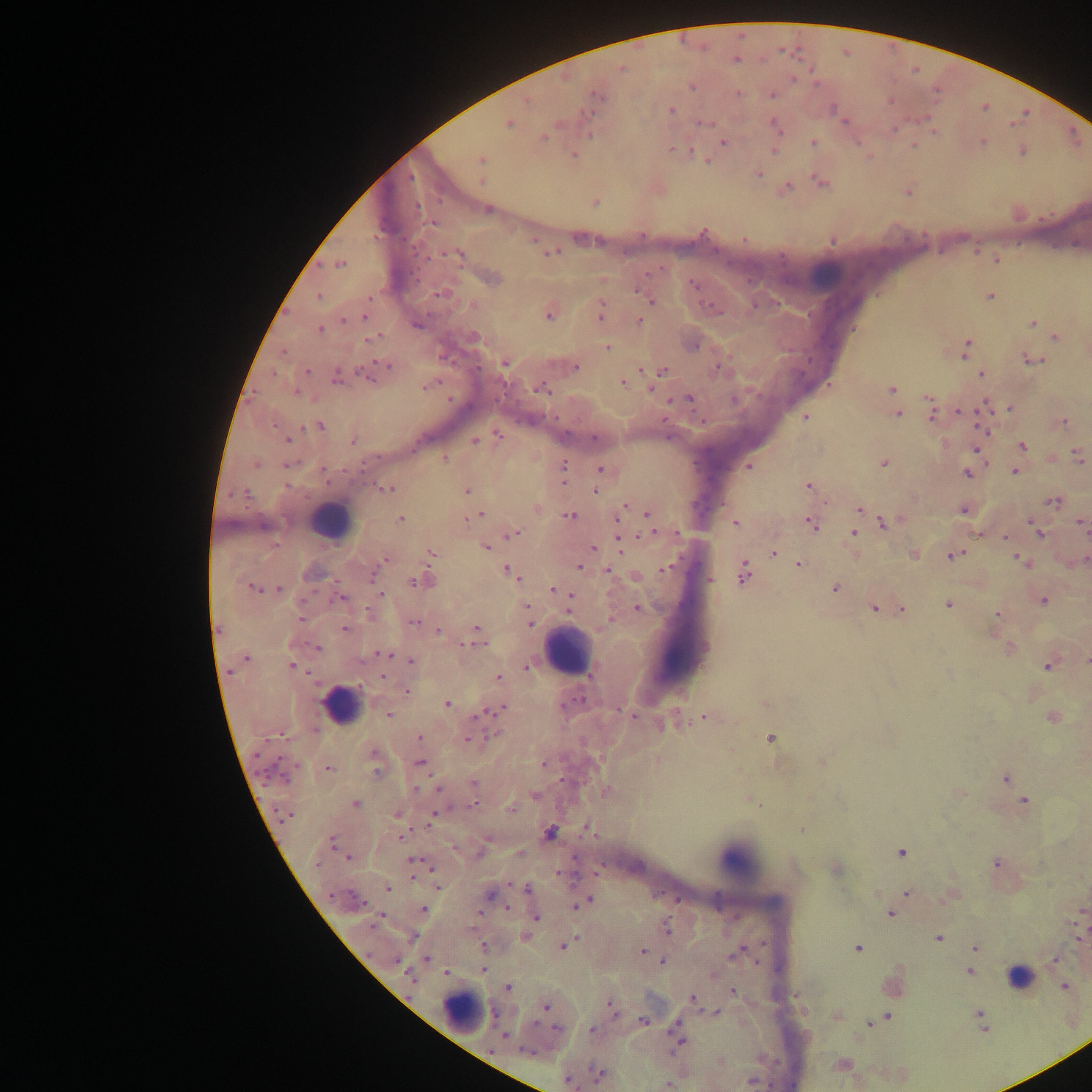 Approximate centers as [x, y] in pixels. Leukocyte locations: [819, 276], [330, 521], [568, 651], [340, 705], [739, 860], [1019, 979], [464, 1012]. Malaria parasite locations: [736, 60], [621, 68], [794, 79], [691, 87], [738, 93], [597, 95], [771, 95], [527, 101], [671, 109], [508, 123], [704, 123], [774, 125], [894, 129], [933, 129], [589, 135], [543, 138], [723, 143], [813, 143], [983, 143], [914, 145], [671, 149], [1021, 150], [773, 151], [574, 155], [480, 160], [707, 160], [760, 173], [821, 183], [787, 186], [595, 203], [487, 210], [433, 223], [703, 232], [744, 239], [551, 253], [459, 254], [995, 260], [340, 265], [653, 270], [493, 278], [694, 284], [442, 293], [641, 293], [319, 296], [989, 296], [649, 300], [548, 316], [601, 316], [364, 317], [344, 321], [639, 321], [1033, 322], [418, 325], [319, 329], [474, 336], [373, 338], [1055, 338], [695, 346], [607, 348], [966, 348], [283, 352], [1032, 360], [505, 363], [388, 366], [575, 367], [718, 368], [307, 371], [662, 371], [364, 373], [275, 375], [982, 375], [336, 379], [623, 382], [426, 386], [541, 388], [650, 388], [892, 390], [295, 392], [688, 399], [734, 400], [985, 405], [1009, 408], [960, 411], [898, 415], [932, 415], [805, 417], [1063, 422], [319, 426], [982, 433], [498, 435], [594, 437], [287, 440], [353, 441], [475, 441], [1023, 445], [976, 449], [1078, 456], [444, 459], [884, 462], [255, 464], [289, 465], [564, 466], [749, 467], [600, 470], [324, 471], [1015, 472], [967, 473], [807, 486], [387, 489], [466, 491], [595, 491], [244, 493], [1054, 501], [623, 507], [963, 510], [859, 511], [621, 512], [648, 513], [479, 515], [570, 515], [473, 516], [401, 520], [883, 521], [735, 523], [1083, 523], [812, 524], [618, 525], [676, 533], [854, 533], [1039, 533], [513, 534], [1005, 538], [619, 542], [485, 547], [593, 547], [773, 552], [431, 553], [954, 555], [1020, 560], [381, 563], [799, 565], [579, 567], [666, 568], [377, 569], [607, 570], [509, 571], [743, 573], [636, 577], [710, 580], [416, 582], [252, 588], [279, 589], [553, 589], [835, 589], [561, 592], [382, 594], [570, 596], [342, 597], [1043, 601], [948, 605], [637, 608], [874, 608], [901, 609], [527, 611], [997, 614], [301, 619], [414, 622], [530, 623], [476, 628], [344, 629], [219, 630], [438, 631], [471, 645], [318, 648], [386, 654], [246, 658], [411, 661], [1086, 661], [292, 666], [1048, 666], [526, 668], [589, 675], [383, 676], [497, 677], [408, 691], [764, 703], [447, 704], [497, 710], [623, 711], [488, 712], [629, 714], [388, 715], [478, 715], [705, 718], [662, 727], [495, 734], [419, 738], [770, 738], [468, 739], [374, 752], [420, 763], [544, 764], [329, 769], [376, 771], [1005, 778], [473, 784], [416, 789], [438, 789], [535, 795], [1023, 801], [355, 804], [755, 804], [473, 805], [512, 809], [284, 815], [396, 815], [431, 819], [587, 828], [801, 830], [549, 833], [401, 837], [332, 842], [901, 852], [519, 854], [347, 858], [414, 860], [997, 864], [317, 865], [413, 876], [438, 887], [387, 888], [528, 888], [907, 893], [490, 896], [358, 900], [581, 903], [507, 907], [424, 909], [891, 914], [536, 918], [666, 928], [412, 937], [526, 937], [938, 938], [1078, 938], [566, 944], [858, 949], [975, 949], [642, 951], [737, 953], [427, 959], [395, 960], [1054, 960], [663, 962], [484, 970], [970, 972], [446, 973], [409, 977], [508, 987], [1065, 987], [733, 991], [692, 997], [546, 1007], [611, 1007], [979, 1012], [717, 1013], [887, 1017], [644, 1021], [869, 1023], [676, 1027], [557, 1029], [591, 1030], [505, 1036], [679, 1040], [527, 1052], [598, 1073], [567, 1080], [752, 1081], [668, 1084]. Image is 1092×1092 pixels. Single field of view. Sample from Ghana. Thick blood film. Mobile-phone photograph taken through the microscope.